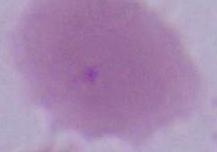
Captured at 1000x magnification. An erythrocyte is shown. Micrograph.